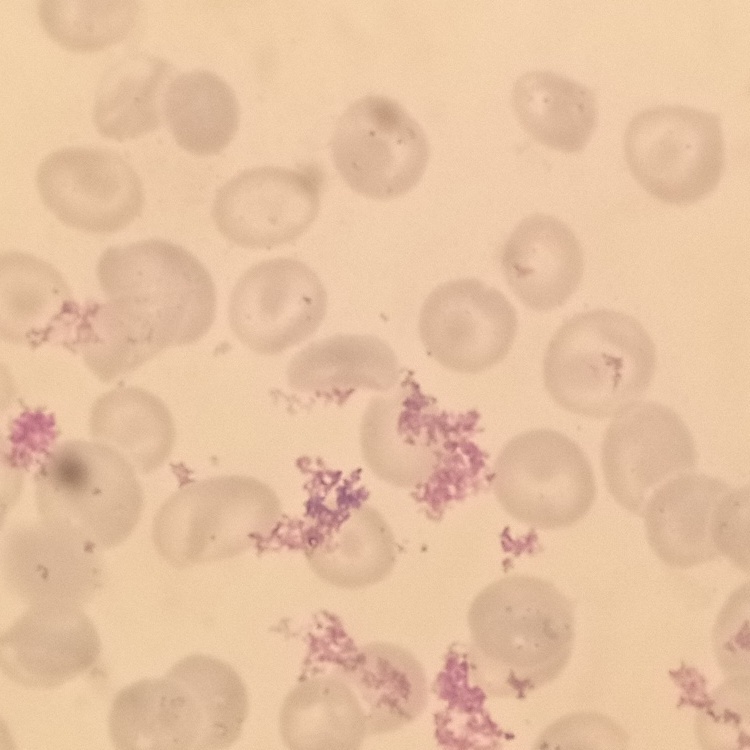 The erythrocytes exhibit no rouleaux formation. Field's or Giemsa stain. Thin blood film. One tile cut from a larger photomicrograph.